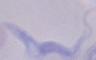

A trypanosome is seen. Captured at 1000x magnification. Photomicrograph.